Give the extent of all Plasmodium ovale-infected red blood cells.
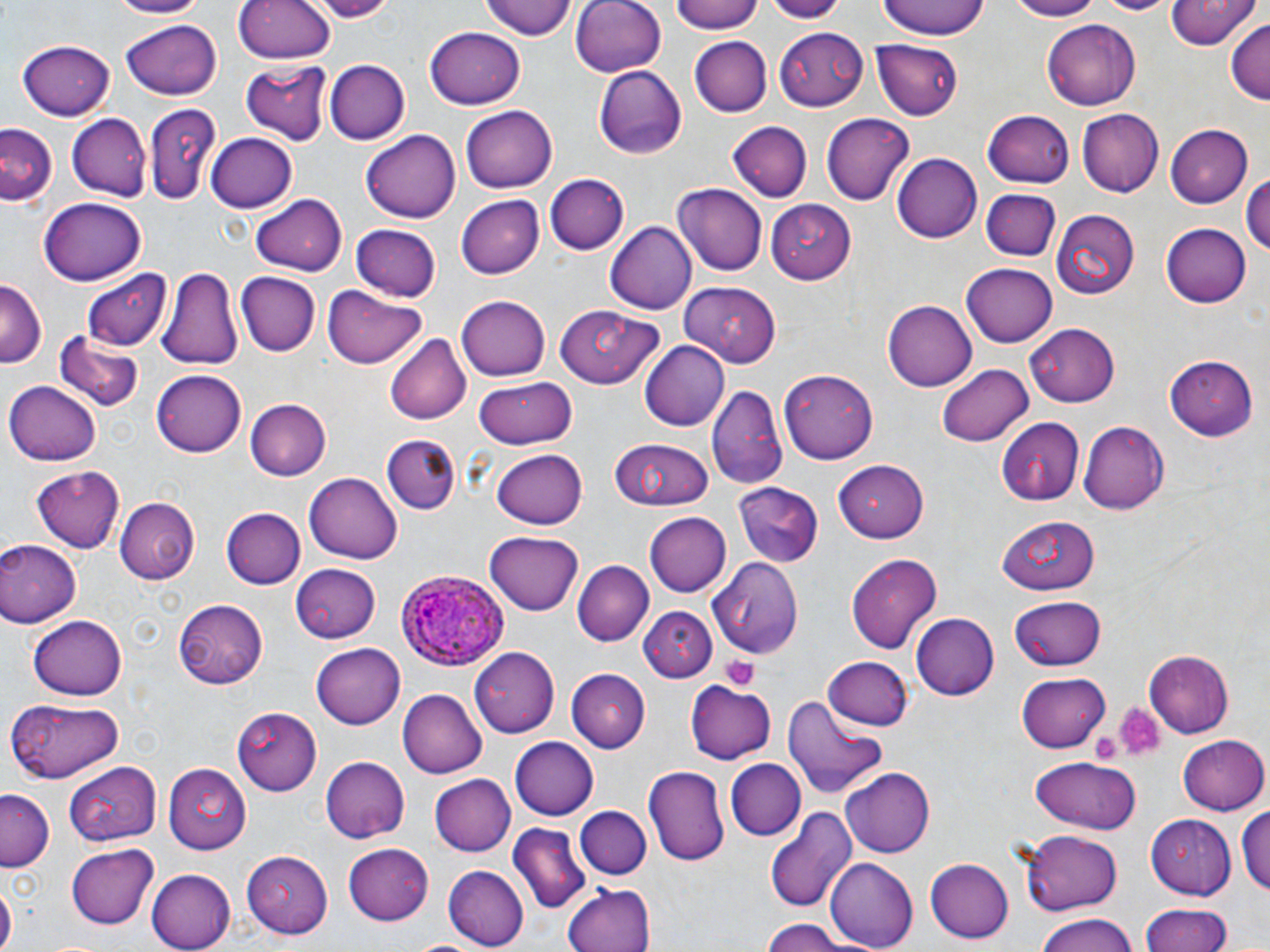

Approximate bounding boxes as [x1, y1, x2, y2] in pixels.
Plasmodium ovale-infected red blood cells: [399, 569, 509, 669].

Uninfected red blood cell locations: [102, 0, 210, 19], [310, 0, 400, 22], [482, 0, 578, 41], [568, 0, 667, 76], [671, 0, 767, 34], [760, 0, 847, 21], [875, 0, 990, 41], [1003, 0, 1108, 21], [1091, 0, 1175, 16], [1164, 0, 1257, 50], [233, 1, 335, 63], [122, 17, 222, 101], [1043, 19, 1140, 111], [1225, 19, 1270, 106], [425, 27, 527, 110], [775, 27, 868, 110], [690, 36, 771, 115], [872, 40, 963, 121], [15, 41, 118, 120], [328, 60, 408, 144], [240, 62, 329, 143], [594, 66, 687, 159], [143, 101, 223, 206], [461, 102, 558, 192], [1075, 108, 1162, 196], [985, 109, 1073, 187], [822, 113, 914, 206], [66, 114, 150, 202], [727, 123, 812, 200], [1, 124, 58, 208], [1168, 124, 1255, 207], [360, 130, 461, 223], [206, 131, 298, 212], [895, 152, 983, 243], [1241, 171, 1270, 262], [543, 173, 627, 256], [674, 184, 767, 275], [981, 189, 1061, 261], [455, 192, 544, 276], [251, 194, 345, 276], [36, 198, 147, 285], [767, 201, 860, 282], [1051, 207, 1141, 300], [605, 223, 695, 313], [1159, 223, 1249, 308], [351, 225, 440, 301], [960, 264, 1056, 348], [159, 267, 243, 370], [83, 270, 173, 350], [234, 271, 319, 355], [0, 279, 45, 365], [682, 283, 782, 366], [323, 286, 426, 367], [455, 295, 550, 381], [882, 300, 976, 393], [555, 308, 664, 387], [1024, 322, 1120, 407], [57, 330, 144, 413], [386, 331, 472, 425], [639, 341, 729, 430], [1166, 354, 1260, 438], [937, 360, 1035, 446], [782, 368, 878, 462], [153, 369, 248, 457], [473, 374, 580, 450], [5, 379, 101, 466], [710, 383, 789, 489], [246, 399, 331, 479], [995, 417, 1086, 502], [1079, 421, 1167, 516], [381, 429, 463, 516], [609, 437, 715, 512], [491, 447, 588, 529], [831, 459, 929, 542], [27, 466, 126, 555], [305, 471, 403, 565], [736, 485, 823, 566], [115, 495, 201, 586], [220, 507, 304, 589], [644, 511, 730, 596], [994, 514, 1101, 594], [486, 531, 584, 616], [0, 539, 79, 628], [845, 552, 943, 655], [712, 555, 803, 656], [572, 560, 652, 646], [286, 564, 381, 645], [1011, 593, 1106, 670], [173, 598, 267, 688], [640, 605, 716, 683], [30, 613, 128, 699], [911, 614, 998, 701], [310, 642, 404, 727], [469, 646, 562, 736], [1144, 649, 1234, 736], [821, 655, 912, 728], [566, 669, 651, 752], [1016, 674, 1111, 752], [689, 679, 778, 764], [398, 688, 487, 778], [781, 693, 888, 800], [7, 698, 124, 782], [233, 705, 322, 796], [1178, 735, 1270, 817], [510, 737, 598, 820], [319, 756, 408, 844], [1029, 756, 1142, 833], [727, 760, 804, 839], [68, 761, 164, 844], [164, 764, 254, 854], [643, 765, 730, 867], [839, 767, 936, 858], [429, 774, 515, 856], [1, 789, 56, 872], [1240, 801, 1270, 900], [766, 805, 858, 916], [574, 806, 651, 879], [1147, 813, 1235, 902], [507, 822, 590, 917], [1020, 830, 1122, 913], [344, 842, 433, 926], [66, 844, 159, 929], [245, 850, 335, 936], [825, 859, 918, 949], [926, 859, 1014, 943], [145, 866, 234, 951], [442, 866, 528, 949], [563, 881, 657, 952], [0, 884, 16, 952], [1138, 904, 1235, 952], [1031, 914, 1143, 952], [759, 918, 851, 952], [407, 936, 492, 952]. Platelet locations: [722, 656, 762, 690], [1114, 701, 1165, 760], [1090, 727, 1124, 764]. Slide-level diagnosis: Plasmodium ovale. Image is 1270×952 pixels. Single field of view. Thin blood film. Light microscopy. May-Grünwald-Giemsa stain. 1000x magnification.